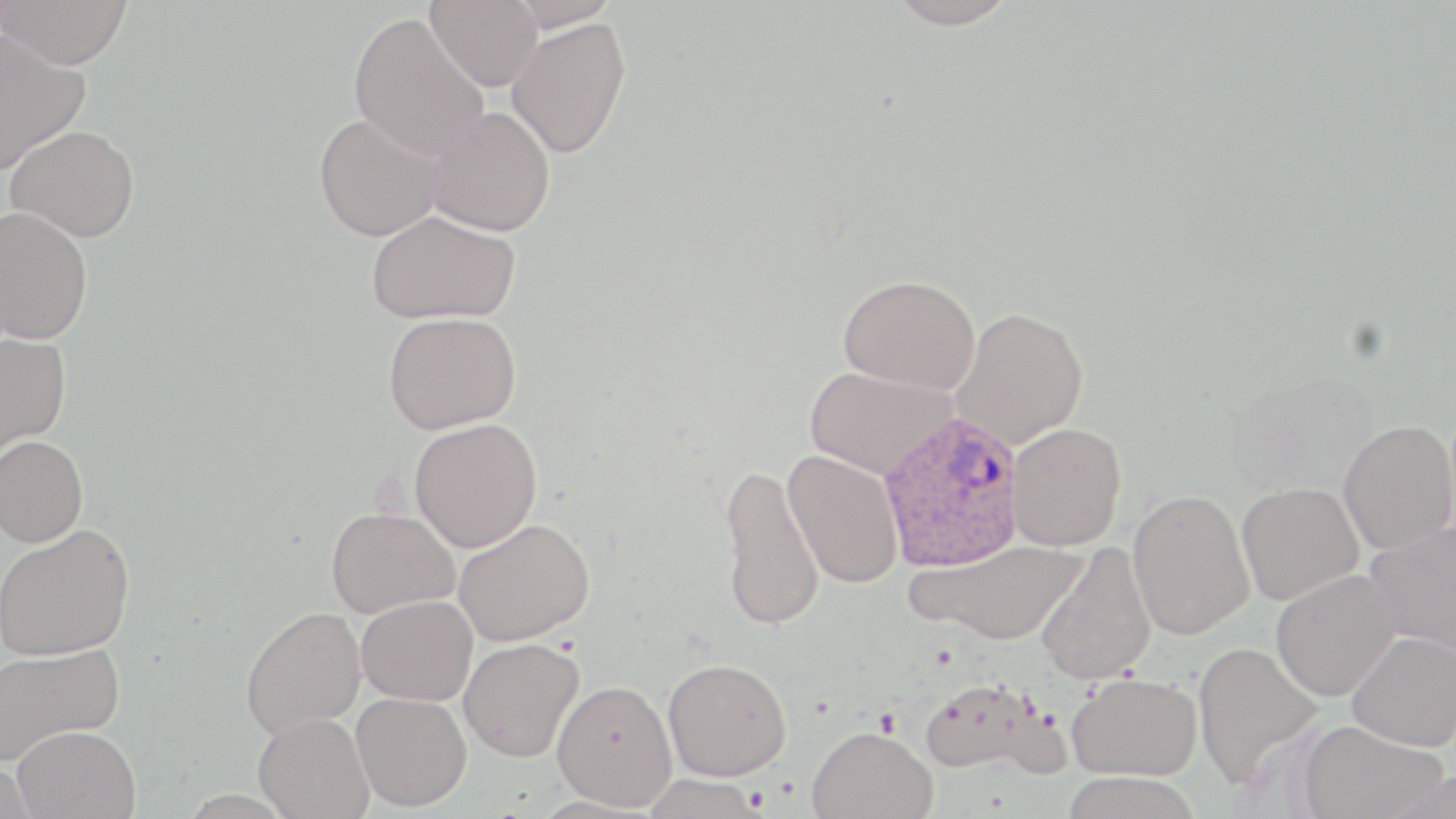

Summary:
  - Coordinate format: approximate bounding boxes as named x1/y1/x2/y2 corners in pixels
  - Plasmodium ovale-infected red blood cell locations: (x1=877, y1=411, x2=1026, y2=571)
  - Uninfected red blood cell locations: (x1=425, y1=0, x2=544, y2=92), (x1=505, y1=0, x2=622, y2=33), (x1=884, y1=0, x2=1018, y2=29), (x1=0, y1=1, x2=136, y2=68), (x1=349, y1=12, x2=490, y2=161), (x1=506, y1=17, x2=632, y2=159), (x1=0, y1=29, x2=89, y2=174), (x1=425, y1=106, x2=555, y2=236), (x1=314, y1=113, x2=443, y2=241), (x1=6, y1=124, x2=140, y2=242), (x1=0, y1=205, x2=94, y2=344), (x1=366, y1=209, x2=521, y2=325), (x1=838, y1=273, x2=980, y2=393), (x1=950, y1=307, x2=1088, y2=449), (x1=383, y1=312, x2=521, y2=434), (x1=0, y1=330, x2=71, y2=460), (x1=804, y1=365, x2=955, y2=479), (x1=409, y1=418, x2=542, y2=553), (x1=1338, y1=420, x2=1456, y2=555), (x1=1007, y1=423, x2=1126, y2=552), (x1=0, y1=435, x2=89, y2=547), (x1=783, y1=449, x2=905, y2=590), (x1=718, y1=463, x2=824, y2=632), (x1=1237, y1=481, x2=1364, y2=605), (x1=1127, y1=488, x2=1255, y2=640), (x1=326, y1=506, x2=460, y2=618), (x1=453, y1=517, x2=594, y2=647), (x1=1364, y1=520, x2=1456, y2=659), (x1=0, y1=524, x2=135, y2=660), (x1=908, y1=538, x2=1089, y2=646), (x1=1035, y1=542, x2=1156, y2=686), (x1=1270, y1=569, x2=1400, y2=701), (x1=356, y1=594, x2=478, y2=706), (x1=240, y1=606, x2=367, y2=738), (x1=1346, y1=630, x2=1456, y2=750), (x1=459, y1=638, x2=584, y2=762), (x1=1192, y1=641, x2=1324, y2=787), (x1=0, y1=643, x2=126, y2=766), (x1=663, y1=657, x2=791, y2=781), (x1=1067, y1=672, x2=1202, y2=780), (x1=917, y1=677, x2=1054, y2=775), (x1=552, y1=678, x2=677, y2=809), (x1=351, y1=691, x2=472, y2=811), (x1=253, y1=712, x2=374, y2=819), (x1=1297, y1=719, x2=1448, y2=819), (x1=12, y1=725, x2=140, y2=818), (x1=807, y1=725, x2=937, y2=819), (x1=1060, y1=771, x2=1204, y2=819), (x1=640, y1=774, x2=768, y2=818)
  - Slide-level diagnosis: Plasmodium ovale
  - Preparation: thin blood smear
  - Image size: 1456×819 pixels
  - Field of view: one of a larger specimen
  - Modality: light microscopy
  - Magnification: 1000x
  - Stain: May-Grünwald-Giemsa